Assess the morphology of the red blood cells.
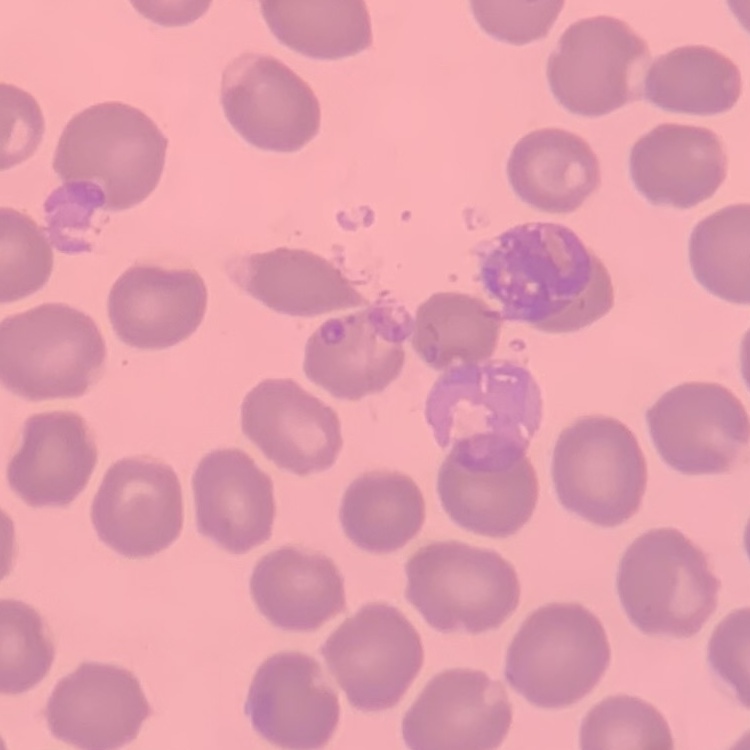

No rouleaux formation.

Summary:
  - Stain: Field's or Giemsa
  - Preparation: thin peripheral smear
  - Image type: one tile cut from a larger photomicrograph